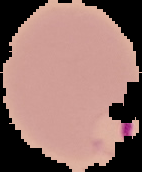
Summary:
  - Malaria status: parasitized
  - Image size: 142×172 pixels
  - Image type: segmented cell region with the area outside set to black
  - Preparation: thin blood film